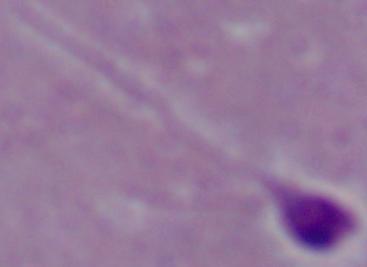

Summary:
  - Magnification: 1000x
  - Modality: micrograph
  - Identification: Leishmania